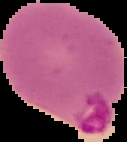

preparation: thin blood film
image_type: cell region segmented out of the field of view; surrounding area masked to black
image_size: 127×142 pixels
malaria_status: parasitized